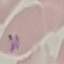
Result: malaria parasites identified. Thin smear of blood. Cell patch, automatically extracted from a larger field of view and resized to 64 × 64 pixels. Acquired by smartphone through the microscope eyepiece. Giemsa-stained preparation.